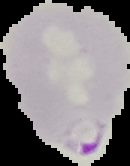

preparation = thin blood smear
malaria status = parasitized
image type = segmented cell region with the area outside set to black
image size = 130×166 pixels